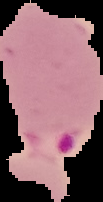
{
  "result": "Plasmodium parasites identified",
  "preparation": "thin blood film",
  "image_type": "segmented cell region on a black background",
  "image_size": "103×202 pixels"
}